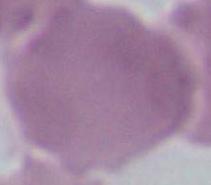

magnification = 1000x
identification = erythrocyte
modality = photomicrograph